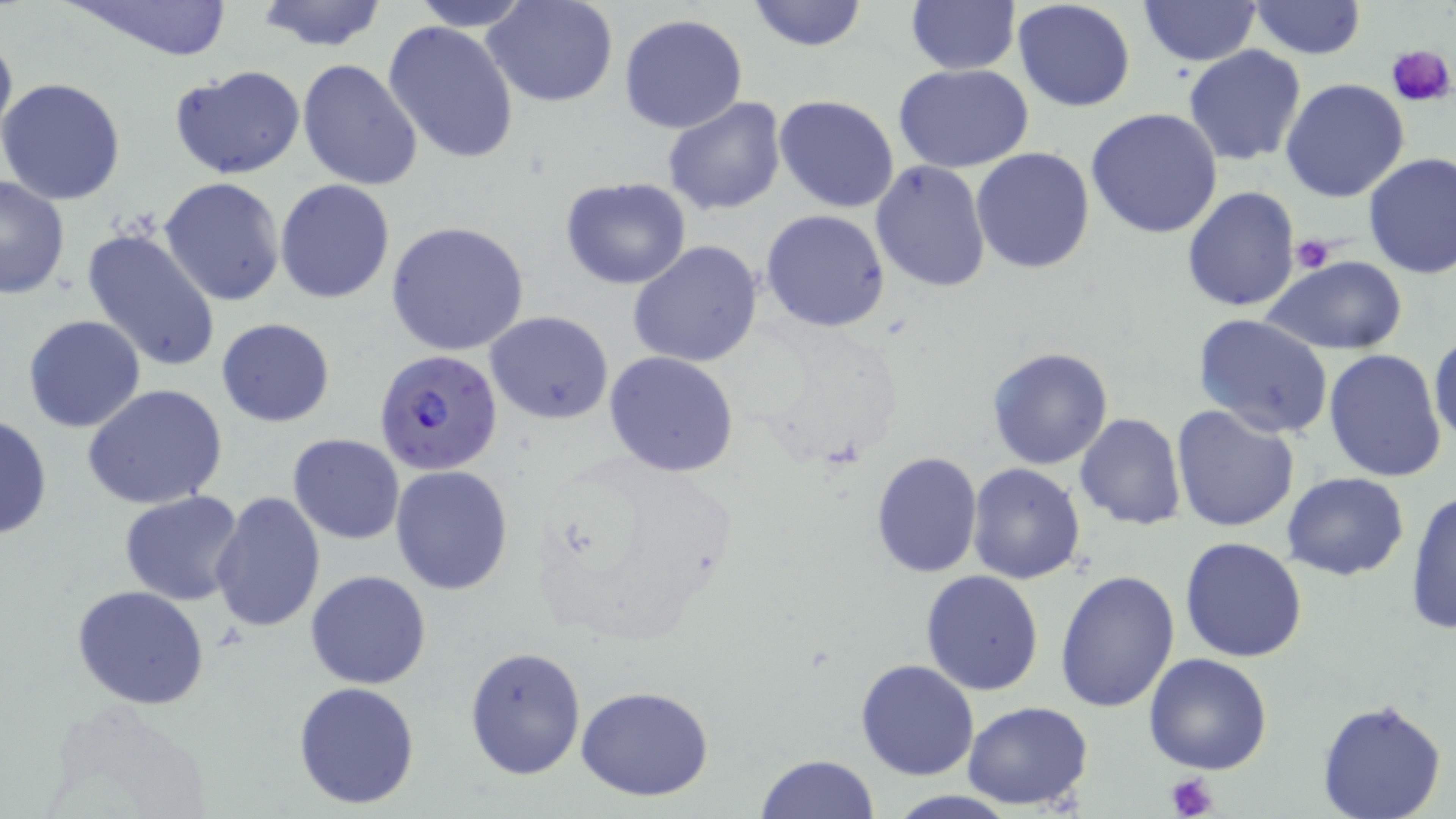

slide-level diagnosis = Plasmodium falciparum
image size = 1456×819 pixels
field of view = single
uninfected red blood cell locations = approximate bounding boxes as (x1, y1, x2, y2) in pixels: (64, 0, 238, 64), (253, 0, 391, 52), (408, 0, 535, 31), (483, 0, 620, 108), (745, 0, 869, 52), (903, 0, 1019, 74), (1012, 0, 1138, 113), (1137, 1, 1261, 67), (1247, 1, 1366, 59), (618, 14, 749, 134), (382, 19, 519, 164), (0, 24, 17, 152), (1183, 45, 1307, 166), (296, 59, 423, 191), (892, 63, 1035, 172), (169, 64, 306, 179), (1280, 77, 1410, 203), (0, 78, 127, 205), (773, 93, 900, 213), (660, 97, 787, 217), (1085, 107, 1223, 240), (971, 147, 1096, 275), (1361, 152, 1456, 279), (869, 161, 991, 293), (0, 175, 72, 302), (159, 176, 287, 308), (560, 177, 692, 290), (275, 180, 395, 303), (1182, 186, 1301, 313), (762, 209, 890, 332), (387, 221, 531, 357), (633, 222, 890, 347), (79, 226, 224, 375), (627, 239, 766, 369), (1262, 257, 1408, 354), (484, 310, 614, 425), (1191, 313, 1335, 441), (22, 314, 146, 433), (215, 318, 335, 428), (1429, 330, 1455, 448), (986, 346, 1113, 469), (1322, 348, 1449, 483), (602, 351, 740, 478), (82, 384, 229, 511), (1170, 404, 1300, 533), (0, 413, 52, 541), (1076, 413, 1188, 530), (288, 434, 406, 544), (528, 453, 736, 650), (870, 453, 982, 578), (390, 464, 514, 596), (967, 464, 1086, 585), (1282, 472, 1410, 580), (1405, 489, 1455, 634), (208, 490, 326, 634), (119, 492, 246, 606), (1180, 536, 1310, 663), (1052, 569, 1181, 713), (304, 570, 432, 691), (920, 570, 1044, 695), (71, 585, 210, 710), (464, 644, 586, 780), (1143, 653, 1273, 774), (856, 660, 979, 781), (293, 680, 420, 809), (574, 685, 716, 802), (1315, 698, 1448, 819), (962, 700, 1094, 810), (755, 753, 877, 819)
preparation = thin blood film
modality = optical microscopy
stain = May-Grünwald-Giemsa
magnification = 1000x
Plasmodium falciparum-infected red blood cell locations = approximate bounding boxes as (x1, y1, x2, y2) in pixels: (373, 347, 504, 477)
platelet locations = approximate bounding boxes as (x1, y1, x2, y2) in pixels: (1387, 43, 1456, 107), (1290, 235, 1337, 275), (1164, 774, 1220, 818)